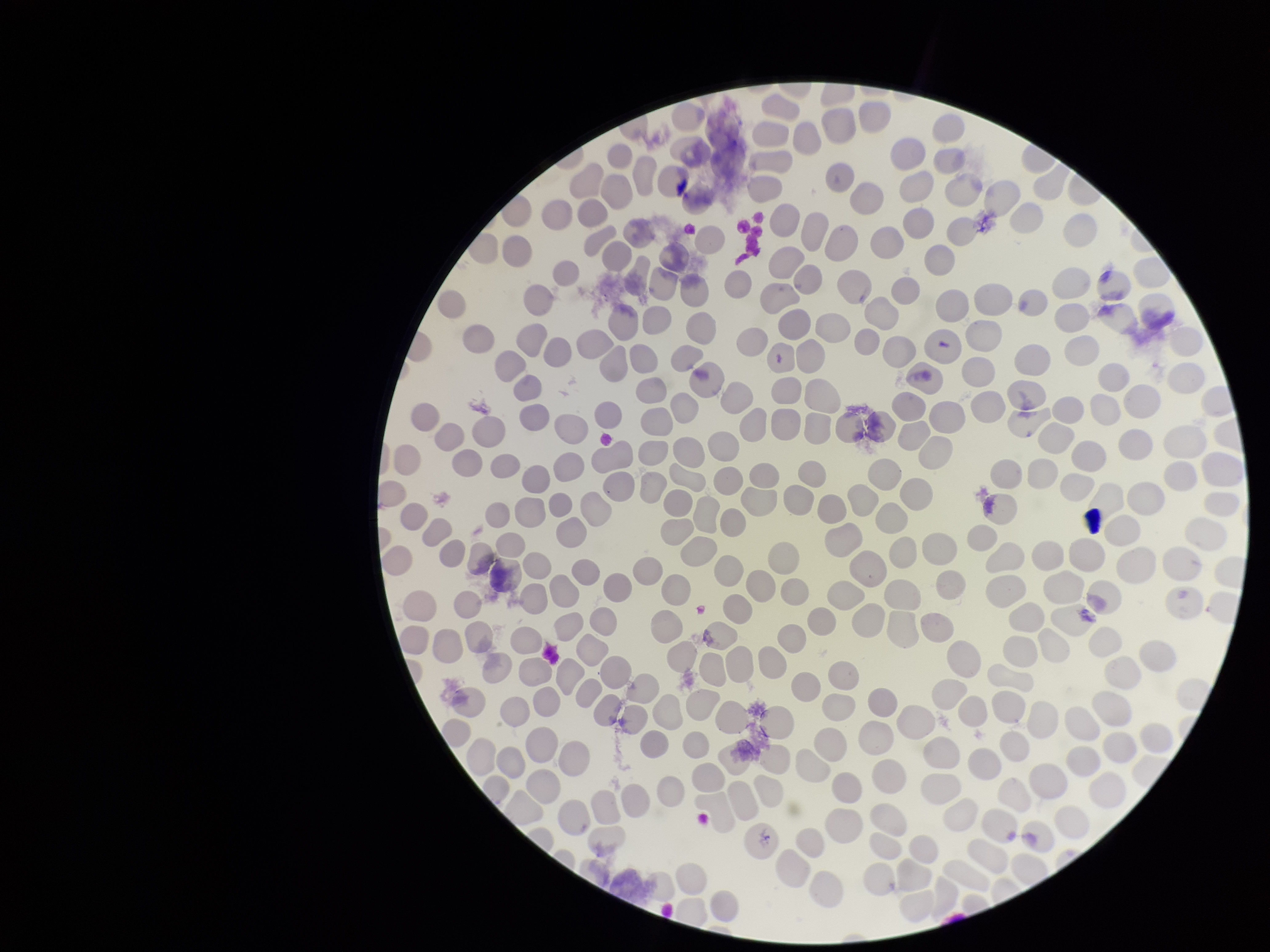 Parasitized red blood cells: none detected. One field from this slide. Image is 1270×952 pixels. Preparation: thin blood smear. Patient malaria status: negative. Parasitized red blood cell count: 0. Giemsa stain. Red blood cell count: 235. Smartphone photograph taken through the eyepiece of a microscope.